Identify the parasite.
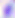
This is Toxoplasma gondii.

magnification = 400x
modality = micrograph